Outline every Plasmodium parasite.
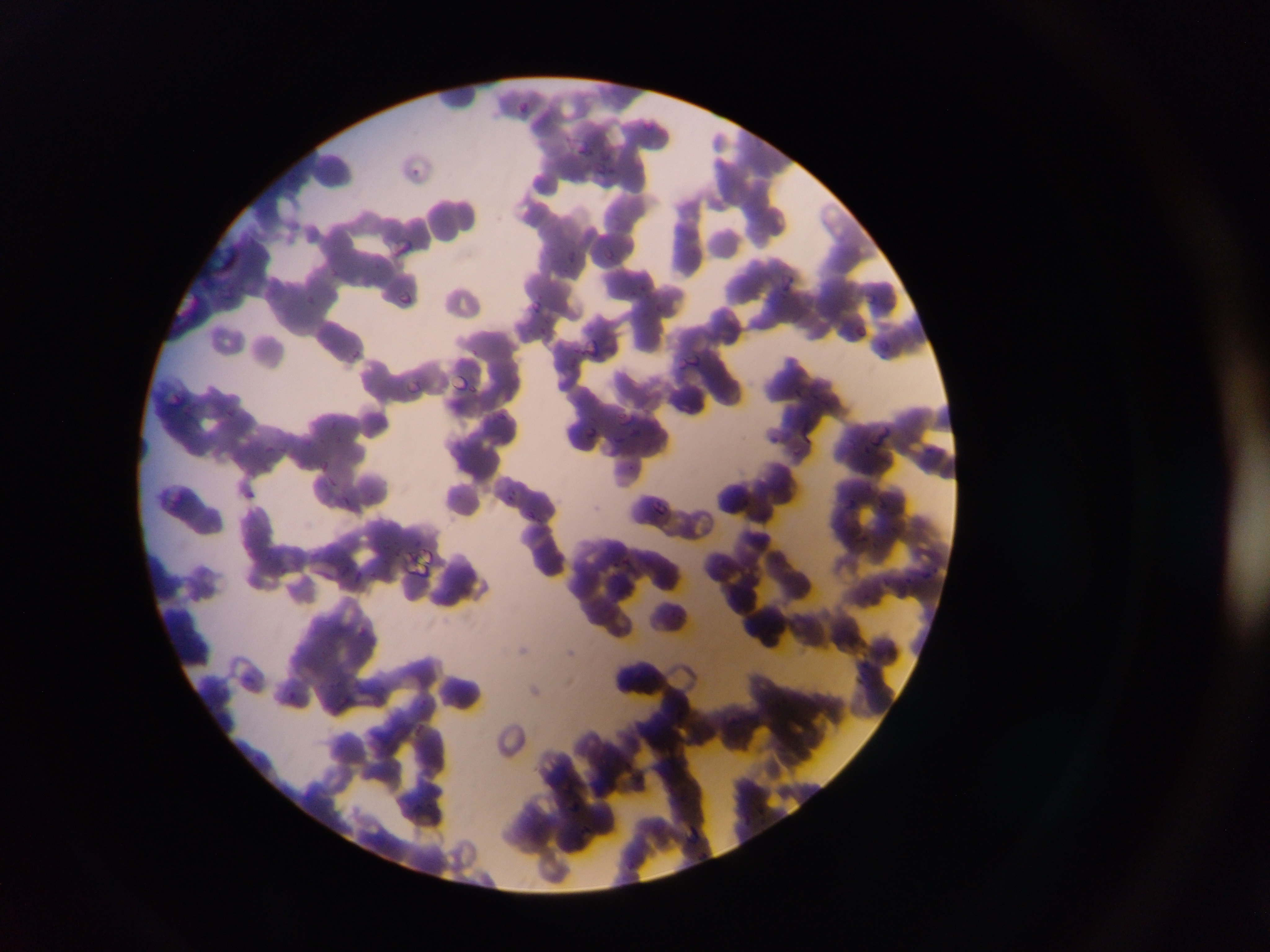
Approximate bounding boxes as left top right bottom in pixels.
Plasmodium parasites: 512 98 533 116; 577 141 601 157; 407 158 432 178; 595 162 614 177; 394 239 416 255; 213 243 242 277; 565 247 576 256; 604 247 617 259; 780 274 794 293; 394 288 409 305; 864 290 885 311; 528 295 550 311; 870 336 900 360; 585 338 599 355; 676 356 702 368; 453 371 471 393; 397 379 427 396; 166 393 185 409; 614 413 644 433; 800 418 823 442; 872 422 898 446; 584 423 597 440; 262 438 275 456; 321 459 332 469; 325 470 348 498; 339 491 356 510; 843 494 859 510; 881 494 894 512; 656 502 675 518; 417 547 439 564; 405 554 435 575; 924 567 938 582; 350 570 368 585; 411 721 429 746; 563 791 579 816; 687 822 707 847.

image size = 1270×952 pixels
capture = mobile-phone photograph through a microscope
country = Ghana
preparation = thin blood smear
field of view = single